Assess this cell for malaria.
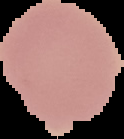
Uninfected.

The area outside the segmented cell region is set to black. From a thin blood smear. Image is 124×139 pixels.